Assess the morphology of the erythrocytes.
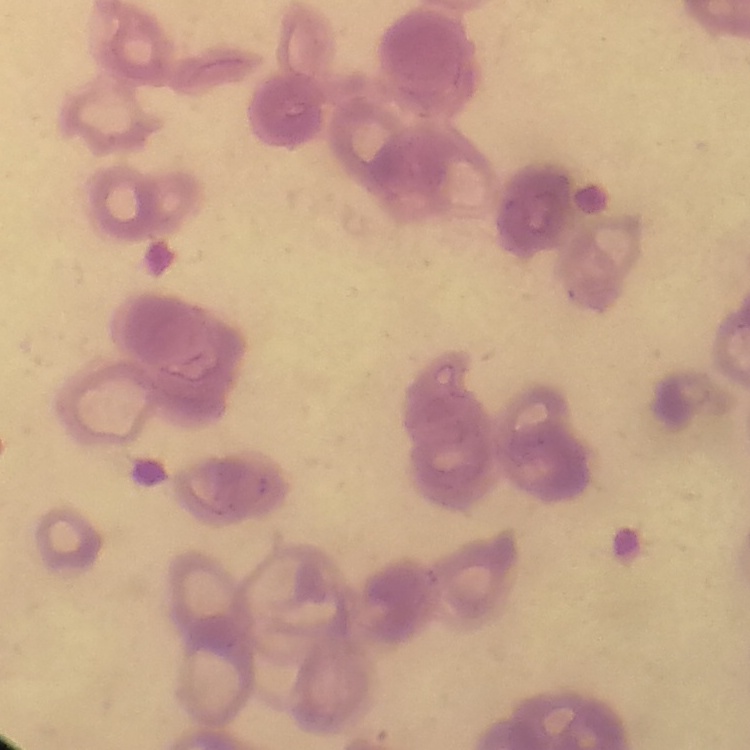
Rouleaux formation.

preparation = thin peripheral smear
stain = Field's or Giemsa
image type = square crop of a larger photomicrograph